Assess this cell for malaria.
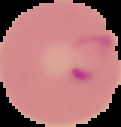
Parasitized.

preparation = thin blood film
image type = segmented cell region on a black background
image size = 121×127 pixels